State which parasite is depicted.
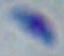

This is Toxoplasma gondii.

Photomicrograph. 1000x magnification.